Comment on the morphology of the erythrocytes.
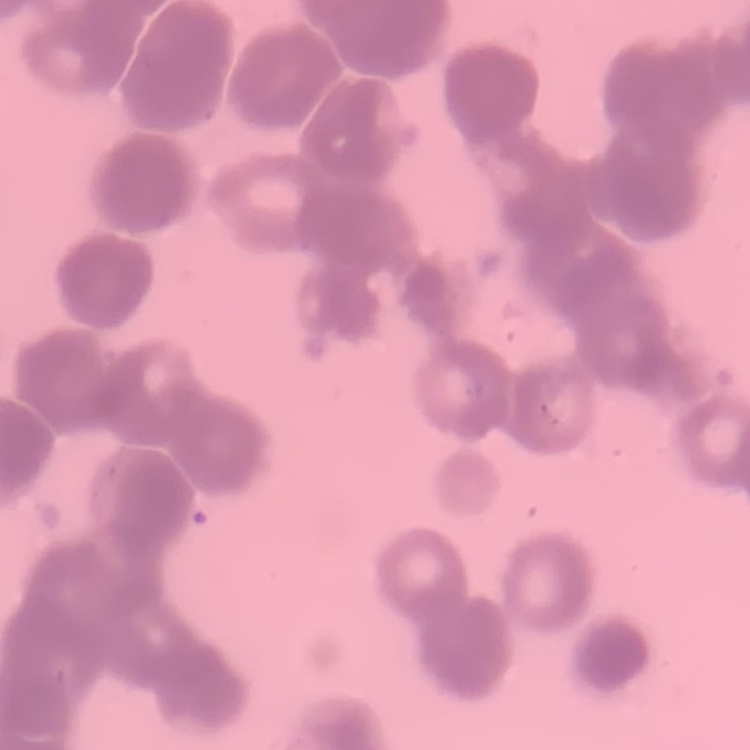

They show rouleaux formation.

Thin blood film. Stained with either Field's or Giemsa. Square crop of a larger photomicrograph.